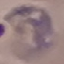
Result: malaria parasites detected. Giemsa stain. Acquired by smartphone through the microscope eyepiece. Thin blood film. Automatically extracted cell patch, resized to 64 × 64 pixels.